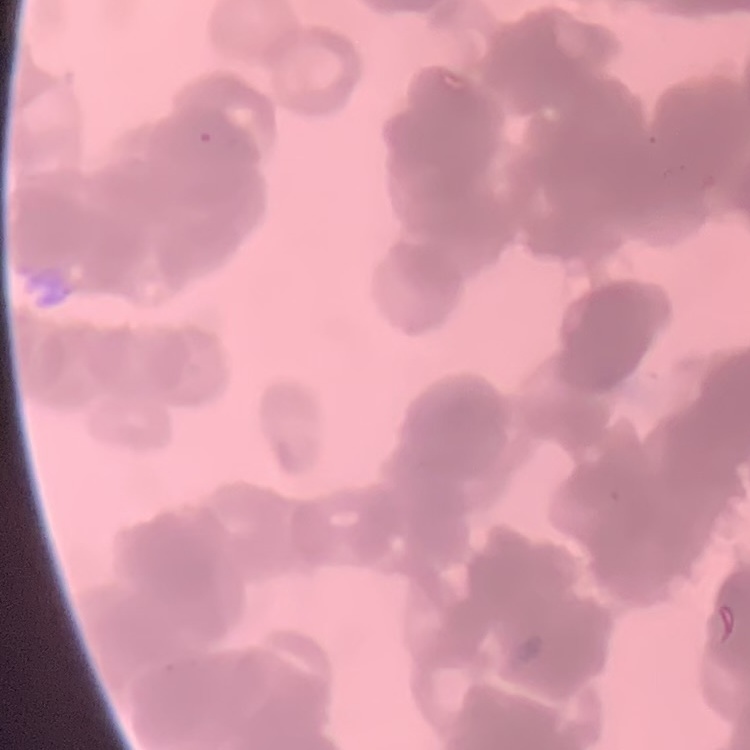

Summary:
  - Erythrocyte morphology: rouleaux formation
  - Image type: one tile cut from a larger photomicrograph
  - Stain: Field's or Giemsa
  - Preparation: thin peripheral smear